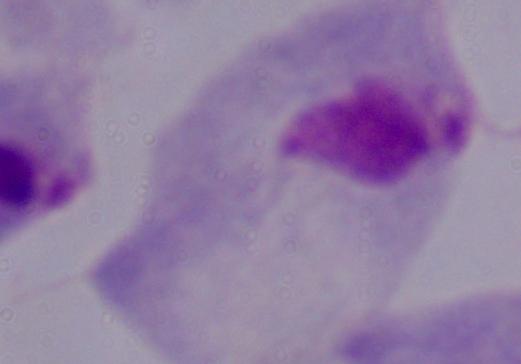
Summary:
  - Magnification: 1000x
  - Modality: photomicrograph
  - Identification: trichomonad